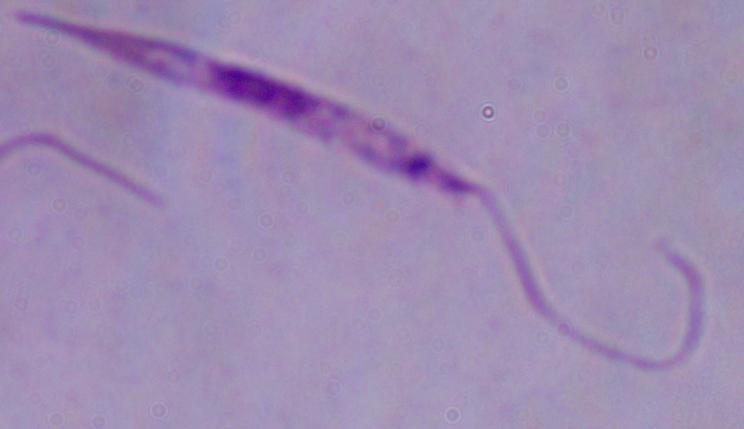

Summary:
  - Identification: Leishmania
  - Modality: photomicrograph
  - Magnification: 1000x